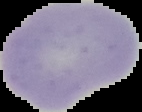

Summary:
  - Result: negative for malaria parasites
  - Image type: segmented cell region on a black background
  - Image size: 142×112 pixels
  - Preparation: thin blood film